Assess for malaria.
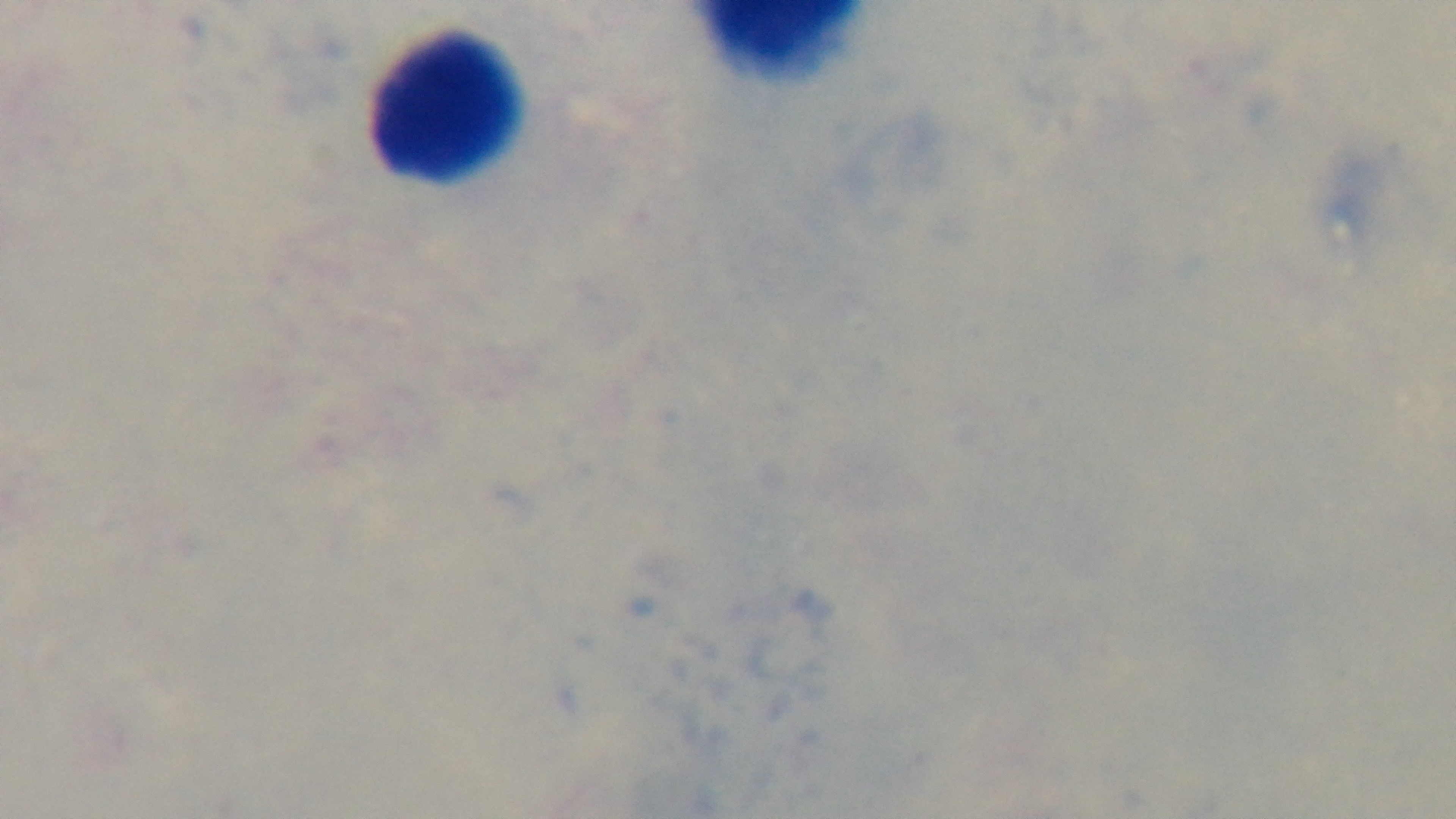

It is uninfected.

Summary:
  - Capture: mounted 4K digital camera
  - Objective: 100x oil immersion
  - Stain: Giemsa
  - Field of view: one from the slide
  - Preparation: thick blood film
  - Modality: light microscopy